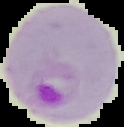

{
  "image_type": "cell region segmented out of the field of view; surrounding area masked to black",
  "result": "Plasmodium parasites identified",
  "preparation": "thin blood smear",
  "image_size": "124×127 pixels"
}